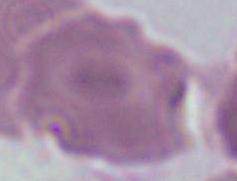

modality = micrograph
magnification = 1000x
identification = red blood cell